State which parasite is depicted.
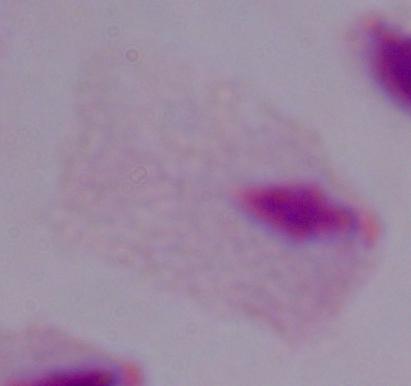
A trichomonad.

Summary:
  - Modality: micrograph
  - Magnification: 1000x